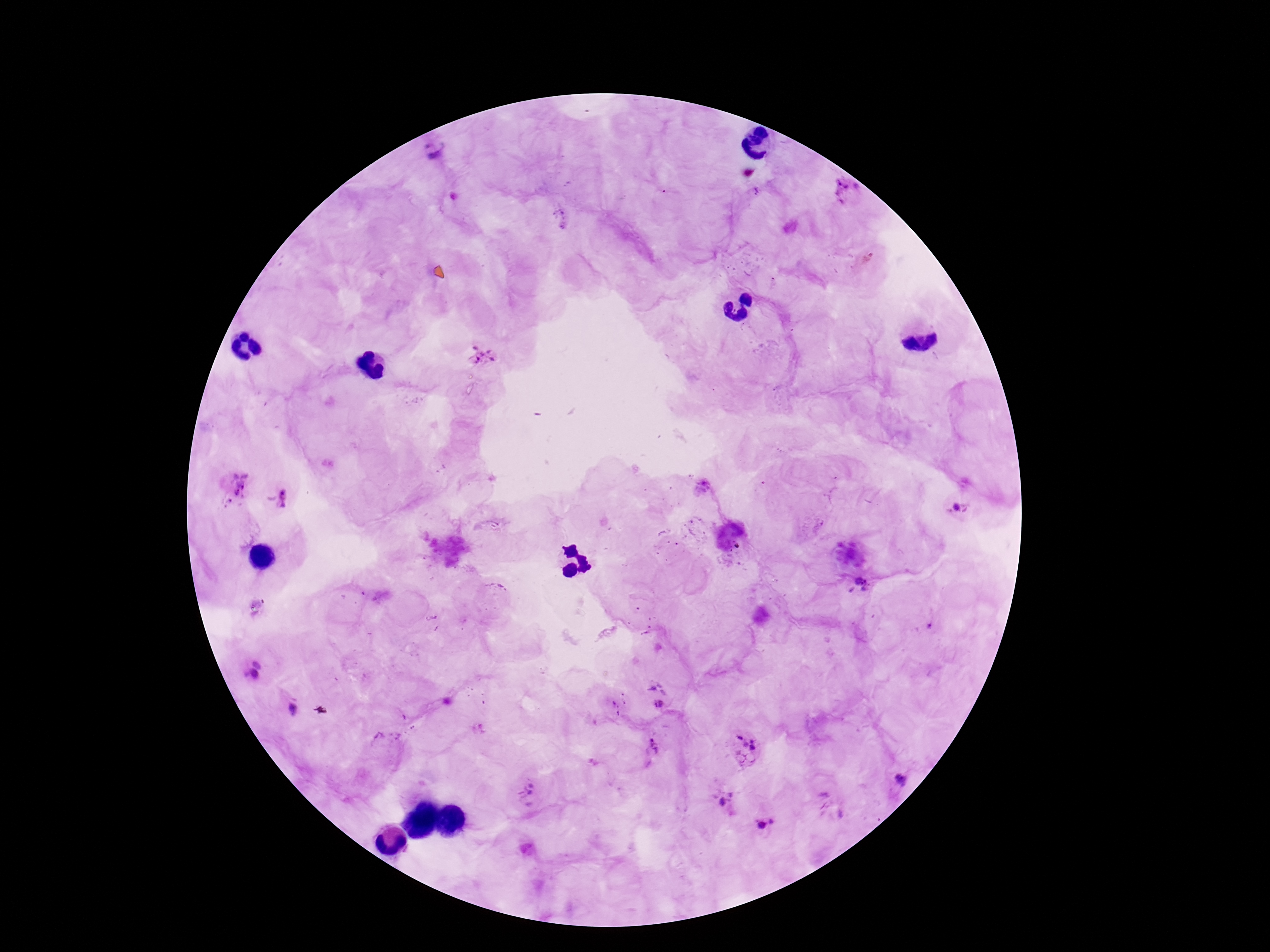
field of view = one from this slide
image size = 1270×952 pixels
patient malaria status = positive
stain = Giemsa
preparation = thick peripheral-blood smear
Plasmodium parasite locations = approximate object centers, in pixels from the top-left corner: (x=432, y=151), (x=845, y=195), (x=483, y=355), (x=235, y=484), (x=281, y=499), (x=959, y=508), (x=860, y=584), (x=258, y=667), (x=655, y=706), (x=290, y=710), (x=745, y=746), (x=652, y=751), (x=902, y=782), (x=529, y=795), (x=722, y=803), (x=767, y=824)
capture = smartphone camera through the microscope eyepiece
magnification = 100x